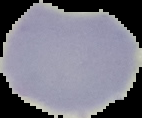 The area outside the segmented cell region is set to black. Result: no malaria parasites detected. From a thin blood smear. Image is 142×118 pixels.